Assess this cell for malaria.
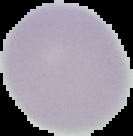
Uninfected.

image size = 133×136 pixels
image type = segmented cell region on a black background
preparation = thin blood smear